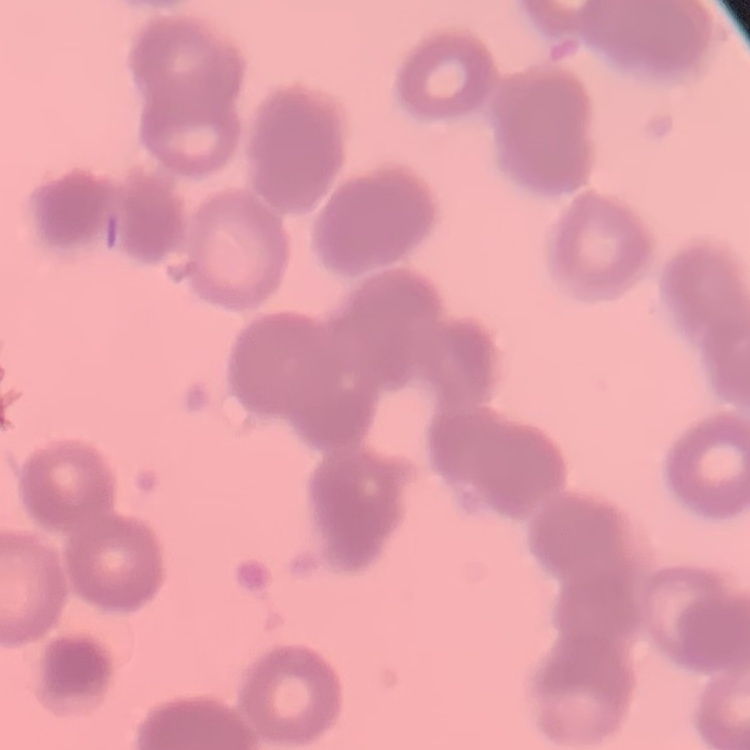
The red blood cells show rouleaux formation. Thin blood film. One tile cut from a larger photomicrograph. Stained with either Field's or Giemsa.